Assess the morphology of the erythrocytes.
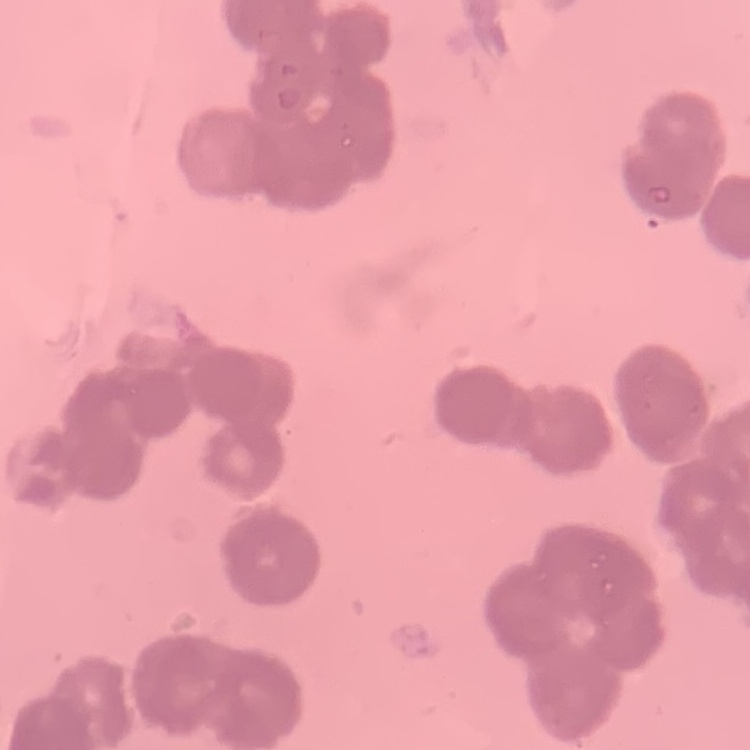

They show rouleaux formation.

Field's or Giemsa stain. One tile cut from a larger photomicrograph. Thin blood film.